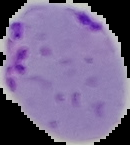 Image is 130×145 pixels. From a thin blood film. Result: Plasmodium parasites detected. Cell region segmented out of the field of view; the surrounding area is masked to black.